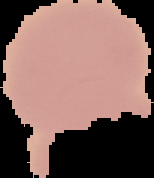 Segmented cell region on a black background. Image is 154×178 pixels. Result: negative for Plasmodium parasites. From a thin blood film.